Classify this cell by malaria status.
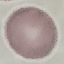

Uninfected.

Summary:
  - Preparation: thin blood film
  - Image type: cell patch, automatically extracted from a larger field of view and resized to 64 × 64 pixels
  - Stain: Giemsa
  - Capture: smartphone through the microscope eyepiece